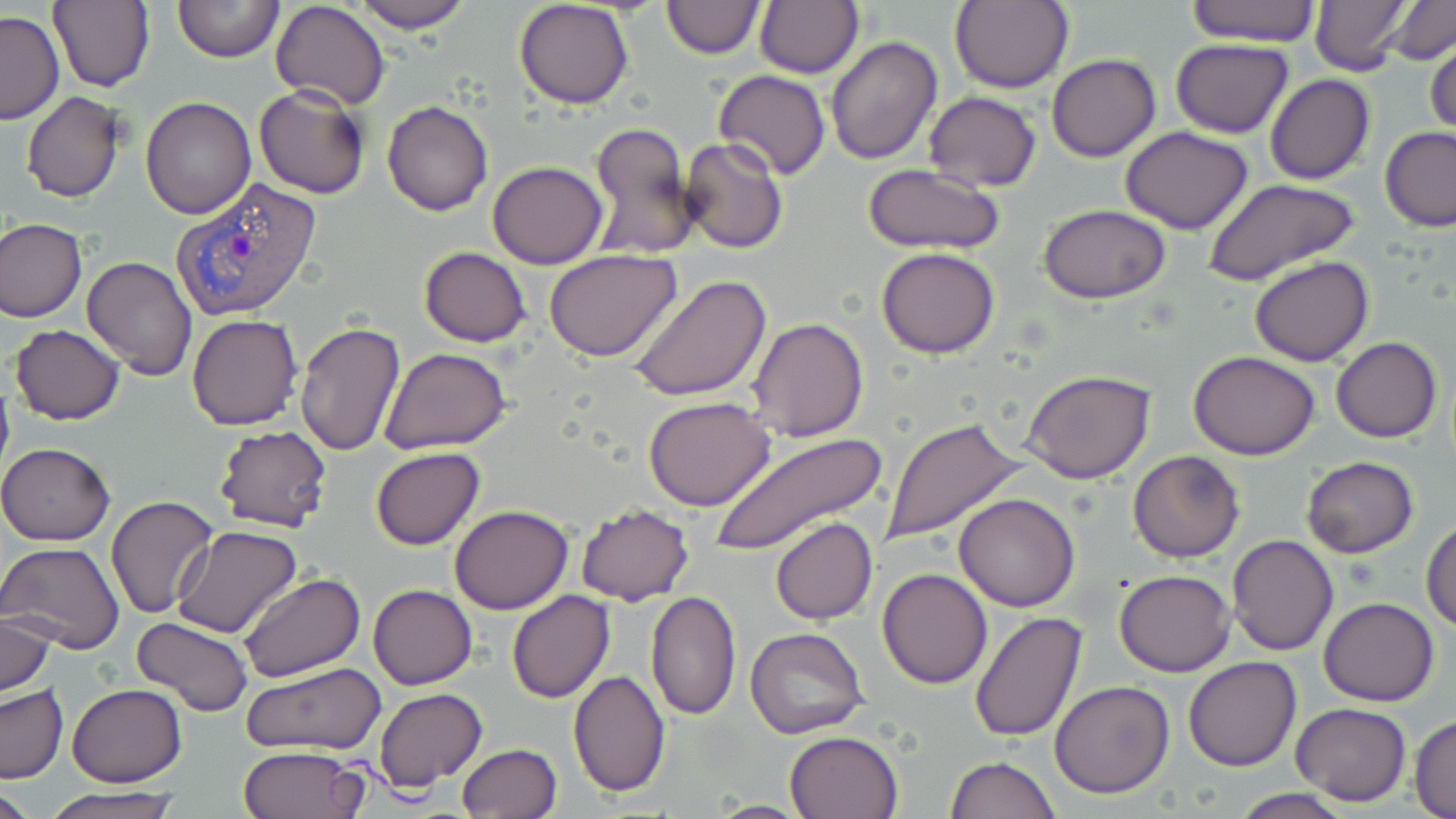

Summary:
  - Coordinate format: approximate bounding boxes as [x1, y1, x2, y2] in pixels
  - Plasmodium vivax-infected red blood cell locations: [170, 176, 324, 324]
  - Uninfected red blood cell locations: [49, 0, 156, 94], [171, 0, 285, 64], [348, 0, 473, 33], [514, 0, 635, 109], [660, 0, 764, 57], [755, 0, 864, 79], [949, 0, 1073, 94], [1185, 0, 1321, 45], [1310, 0, 1414, 76], [1384, 0, 1456, 64], [272, 2, 389, 110], [1, 11, 63, 124], [825, 34, 942, 165], [1425, 36, 1456, 140], [1169, 37, 1294, 138], [1047, 54, 1161, 162], [713, 69, 831, 181], [1264, 73, 1374, 185], [254, 86, 372, 199], [922, 91, 1040, 192], [22, 93, 124, 204], [141, 97, 256, 220], [382, 100, 493, 216], [588, 121, 698, 259], [1120, 125, 1254, 234], [1379, 126, 1456, 231], [679, 136, 790, 256], [488, 161, 608, 269], [861, 164, 1007, 256], [1207, 179, 1361, 287], [1038, 205, 1168, 304], [0, 217, 86, 322], [418, 247, 532, 347], [878, 247, 999, 359], [544, 248, 681, 361], [81, 253, 198, 378], [1249, 257, 1375, 367], [629, 274, 773, 402], [186, 314, 303, 430], [747, 318, 870, 442], [294, 322, 406, 457], [9, 324, 124, 425], [1332, 336, 1442, 441], [378, 348, 512, 455], [1189, 350, 1320, 460], [1021, 368, 1155, 483], [0, 371, 15, 486], [644, 396, 776, 511], [882, 419, 1025, 544], [213, 426, 335, 533], [710, 431, 888, 554], [0, 442, 118, 545], [370, 447, 485, 550], [1128, 450, 1246, 563], [1301, 456, 1418, 558], [953, 493, 1079, 611], [106, 496, 218, 618], [449, 504, 575, 614], [575, 505, 695, 605], [1421, 516, 1455, 633], [770, 518, 877, 624], [173, 524, 302, 639], [1227, 536, 1339, 657], [0, 541, 125, 654], [877, 568, 992, 689], [1113, 569, 1236, 676], [238, 572, 366, 681], [368, 584, 477, 689], [646, 590, 742, 720], [507, 591, 615, 703], [1319, 598, 1440, 706], [0, 609, 56, 700], [969, 610, 1088, 743], [131, 616, 253, 718], [521, 618, 645, 767], [744, 628, 870, 741], [1184, 657, 1301, 771], [241, 662, 386, 756], [567, 669, 670, 798], [1050, 681, 1175, 798], [68, 684, 186, 787], [0, 685, 67, 783], [374, 689, 487, 790], [1291, 701, 1411, 804], [1409, 716, 1455, 819], [785, 730, 904, 819], [457, 743, 562, 818], [238, 745, 370, 819], [946, 756, 1059, 819], [1, 782, 49, 816], [39, 788, 183, 819], [1226, 788, 1355, 819], [703, 800, 813, 817]
  - Slide-level diagnosis: Plasmodium vivax
  - Magnification: 1000x
  - Field of view: one of a larger specimen
  - Image size: 1456×819 pixels
  - Stain: May-Grünwald-Giemsa
  - Preparation: thin blood smear
  - Modality: light microscopy